Point out each leukocyte.
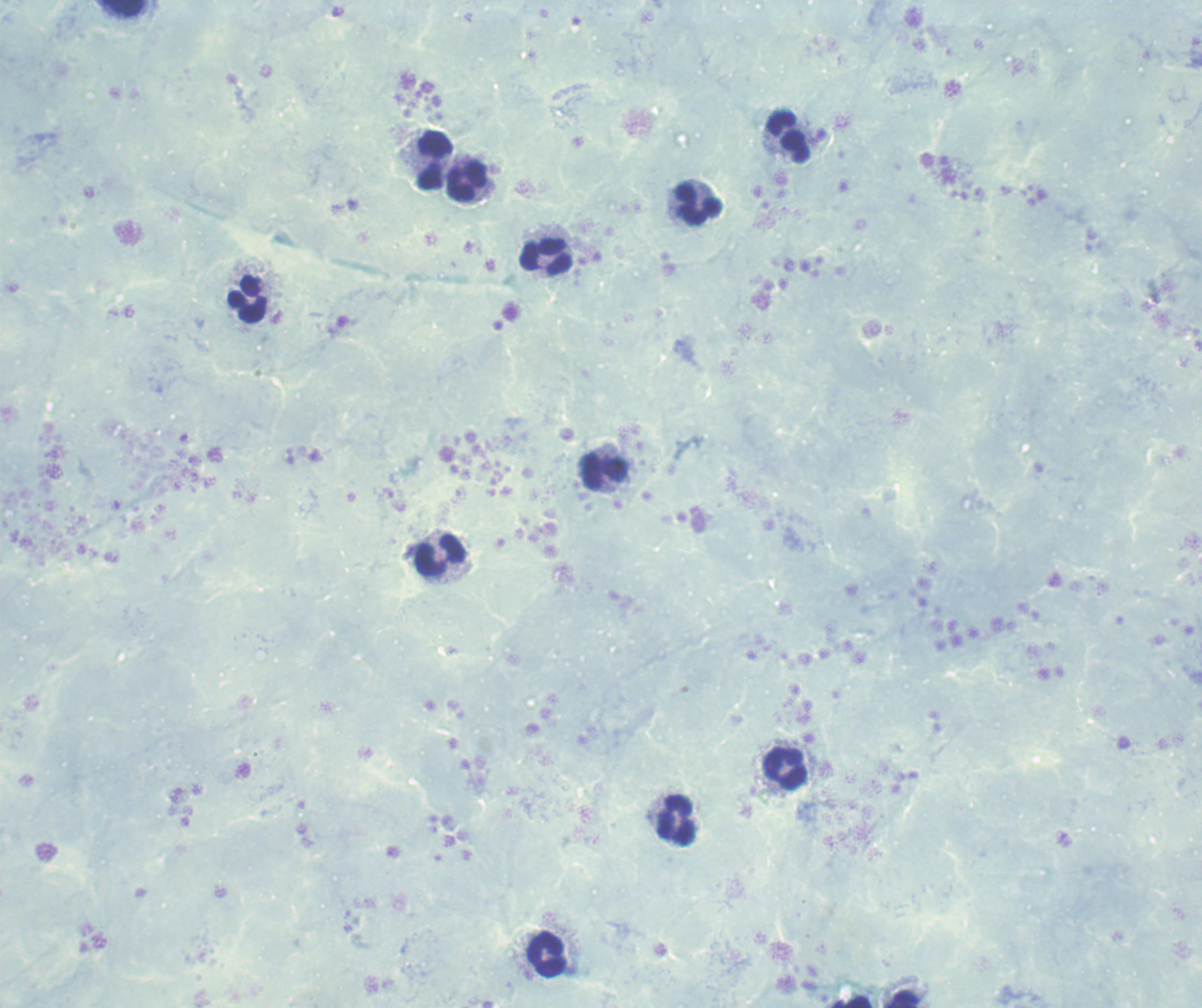

Approximate centers as {x, y} in pixels.
Leukocytes: {123, 8}, {788, 137}, {435, 159}, {467, 181}, {699, 203}, {547, 256}, {247, 299}, {604, 472}, {440, 555}, {785, 769}, {677, 820}, {547, 954}.

Summary:
  - Field of view: one from this slide
  - Preparation: thick blood film
  - Image size: 1202×1008 pixels
  - Background quality: poor
  - Result: no malaria parasites seen
  - Context: previously used in a real diagnosis
  - Magnification: 100x
  - Stain: Romanowsky